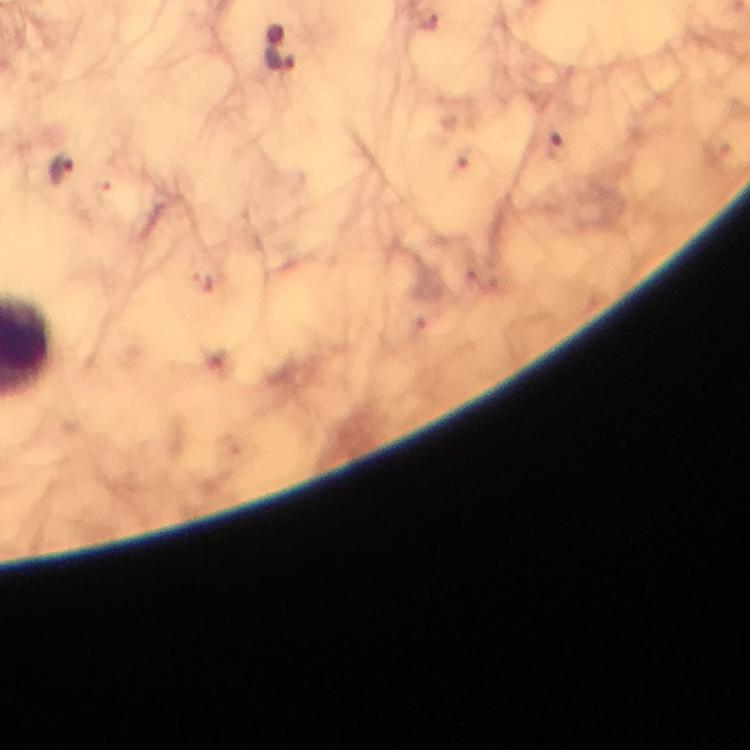
magnification = 100x
immersion oil = used
cropped from = a single field of view
image size = 750×750 pixels
malaria parasite locations = approximate object centers, in pixels from the top-left corner: (x=278, y=58), (x=559, y=145), (x=61, y=168)
stain = Giemsa
preparation = thick smear
context = from a malaria diagnostic workup
capture = smartphone photograph through a microscope